Locate every malaria parasite and identify its life-cycle stage.
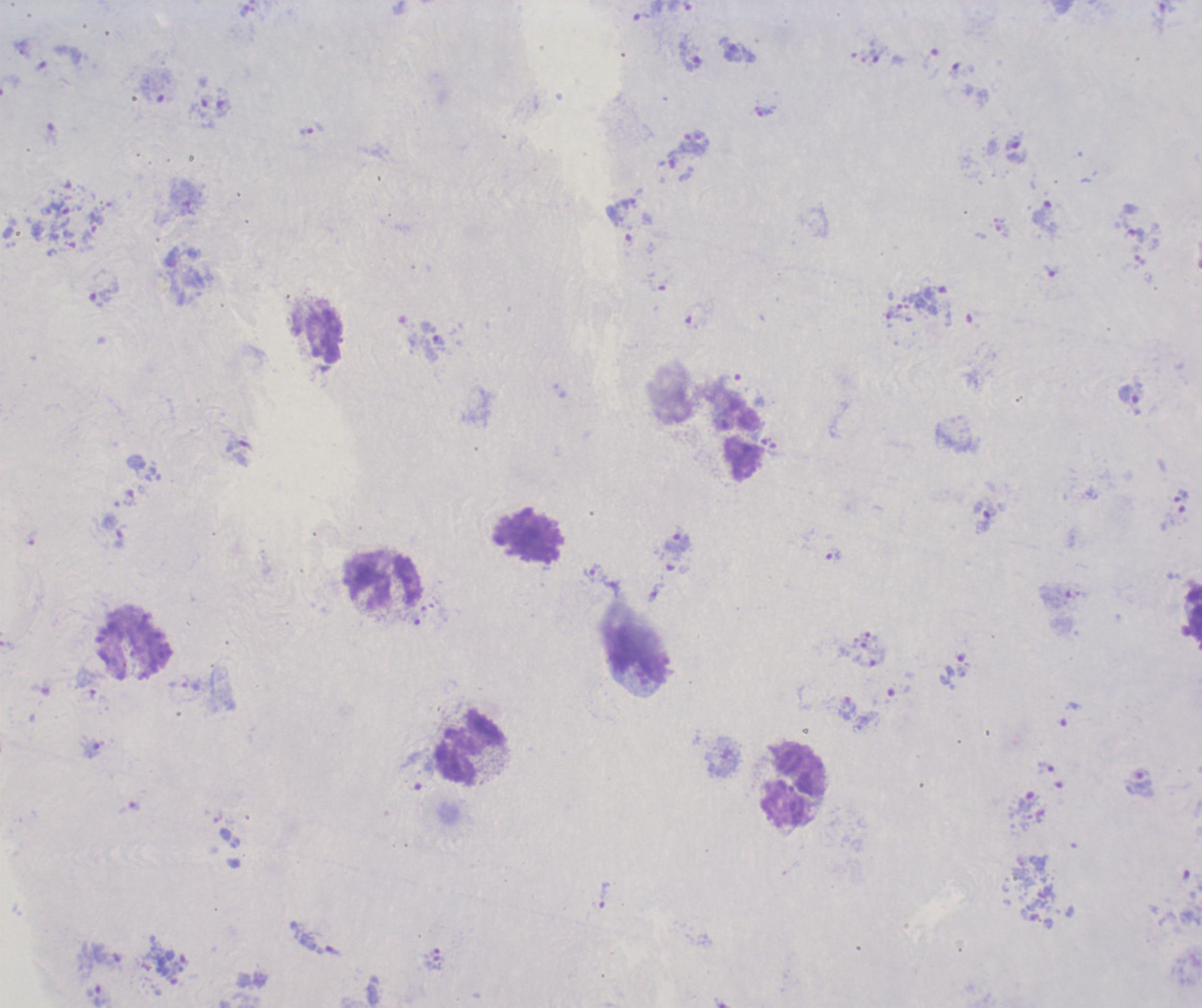

Approximate centers as (x, y) in pixels.
Trophozoites: (732, 52), (690, 56), (1014, 143), (1052, 271), (103, 292), (1129, 395), (1181, 495), (986, 518), (677, 543), (834, 555), (592, 573), (92, 749), (1046, 769), (1028, 802), (605, 895).
No schizont or gametocyte forms observed.

coordinate format = approximate centers as (x, y) in pixels
leukocyte locations = (530, 536), (386, 582), (134, 643), (641, 656), (469, 749), (795, 783)
magnification = 100x
stain = Romanowsky
preparation = thick blood smear
context = previously used in a real diagnosis
image size = 1202×1008 pixels
background quality = unsatisfactory
field of view = single